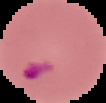
Summary:
  - Result: Plasmodium parasites identified
  - Image type: cell region segmented out of the field of view; surrounding area masked to black
  - Image size: 106×103 pixels
  - Preparation: thin blood smear